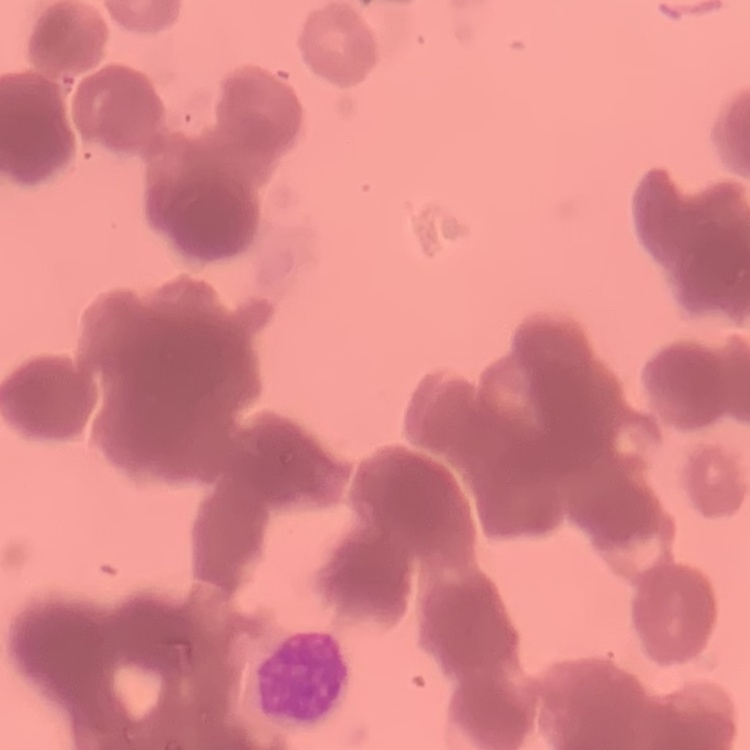

red blood cell morphology = rouleaux formation
stain = Field's or Giemsa
preparation = thin peripheral smear
image type = square crop of a larger photomicrograph